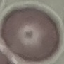
Summary:
  - Malaria status: uninfected
  - Stain: Giemsa
  - Preparation: thin blood smear
  - Image type: automatically extracted cell patch, resized to 64 × 64 pixels
  - Capture: smartphone camera at the microscope eyepiece